Locate and identify every blood parasite.
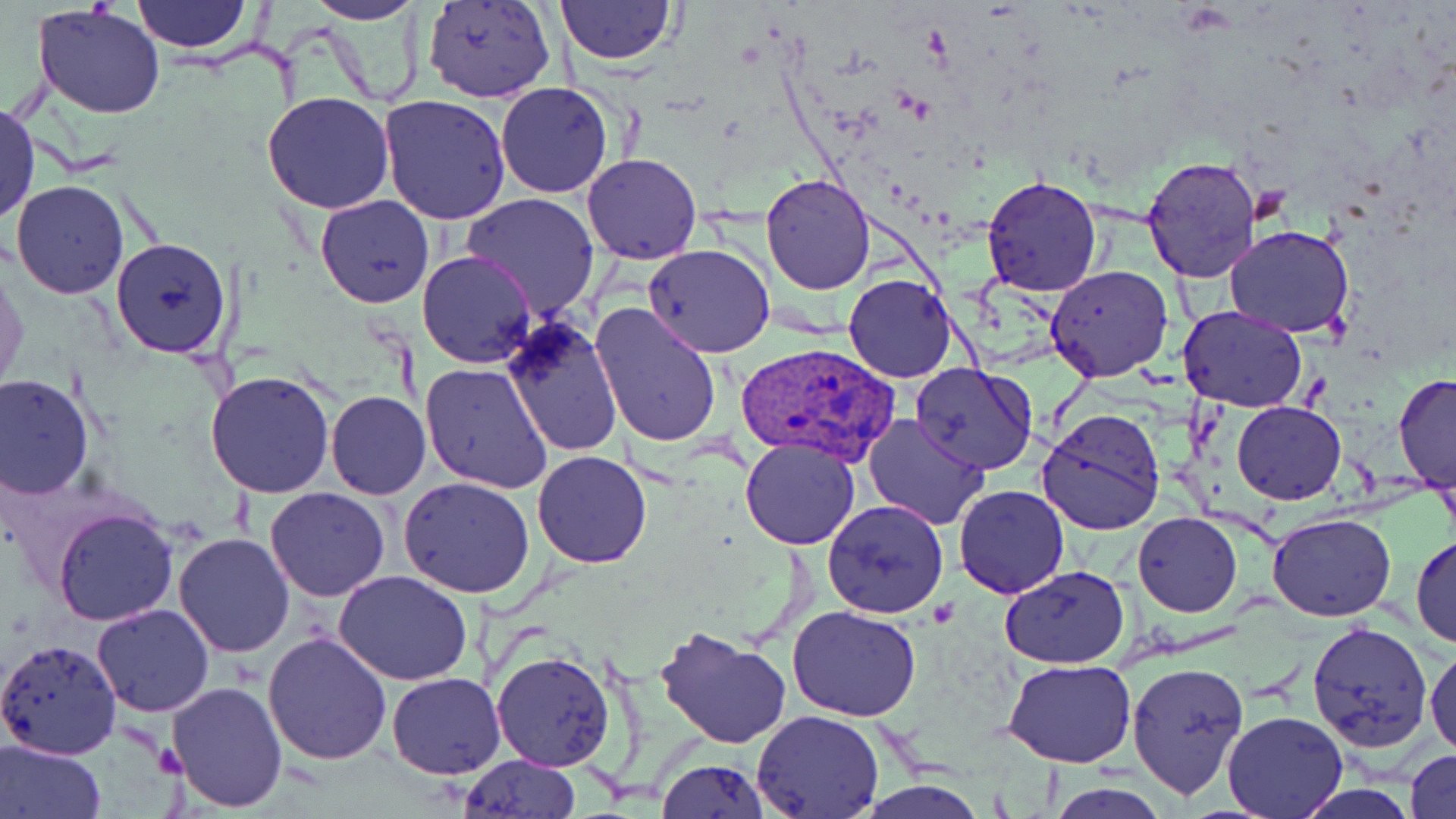

Approximate bounding boxes as (x1, y1, x2, y2) in pixels.
Plasmodium vivax-infected red blood cells: (734, 340, 898, 468).
No Plasmodium falciparum, Plasmodium ovale, Plasmodium malariae, Babesia divergens, or Trypanosoma brucei observed.

Uninfected red blood cell locations: (132, 0, 252, 54), (424, 0, 556, 104), (556, 0, 674, 65), (307, 2, 424, 25), (33, 5, 166, 119), (495, 82, 613, 198), (261, 91, 394, 215), (379, 96, 512, 226), (0, 99, 39, 225), (583, 153, 702, 265), (1140, 155, 1263, 284), (761, 173, 875, 293), (981, 174, 1103, 297), (11, 180, 128, 299), (460, 192, 601, 320), (315, 195, 434, 308), (1223, 224, 1354, 338), (110, 237, 232, 357), (643, 244, 774, 356), (417, 250, 536, 368), (1, 265, 28, 392), (1046, 265, 1173, 384), (843, 274, 957, 383), (589, 301, 723, 449), (1179, 305, 1308, 412), (500, 315, 623, 456), (422, 362, 551, 493), (909, 362, 1040, 475), (206, 370, 336, 500), (0, 374, 94, 499), (1393, 374, 1456, 493), (325, 390, 430, 500), (1232, 400, 1345, 504), (1037, 409, 1168, 535), (864, 414, 987, 530), (739, 437, 861, 550), (532, 451, 652, 568), (398, 477, 536, 598), (954, 486, 1070, 598), (265, 487, 391, 602), (822, 500, 949, 620), (52, 507, 178, 626), (1134, 513, 1241, 616), (1267, 513, 1397, 620), (172, 532, 296, 658), (1411, 533, 1456, 651), (999, 565, 1131, 669), (334, 570, 475, 686), (92, 602, 215, 716), (787, 605, 921, 722), (1308, 620, 1433, 750), (654, 624, 793, 750), (262, 631, 392, 766), (1426, 637, 1456, 759), (0, 639, 122, 760), (490, 649, 617, 772), (1003, 659, 1135, 768), (1128, 661, 1250, 799), (387, 673, 505, 778), (166, 680, 286, 810), (1223, 709, 1346, 817), (752, 711, 883, 819), (0, 738, 106, 819), (1407, 749, 1456, 819), (459, 753, 581, 818), (656, 758, 771, 819), (855, 780, 990, 818), (1044, 782, 1172, 819). Platelet locations: (1247, 187, 1290, 225). Slide-level diagnosis: Plasmodium vivax. May-Grünwald-Giemsa stain. Image is 1456×819 pixels. Optical microscopy. Single field of view. Thin blood film. 1000x magnification.